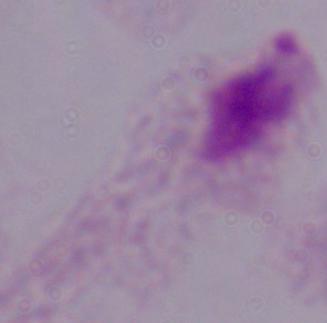
identification: trichomonad
magnification: 1000x
modality: photomicrograph